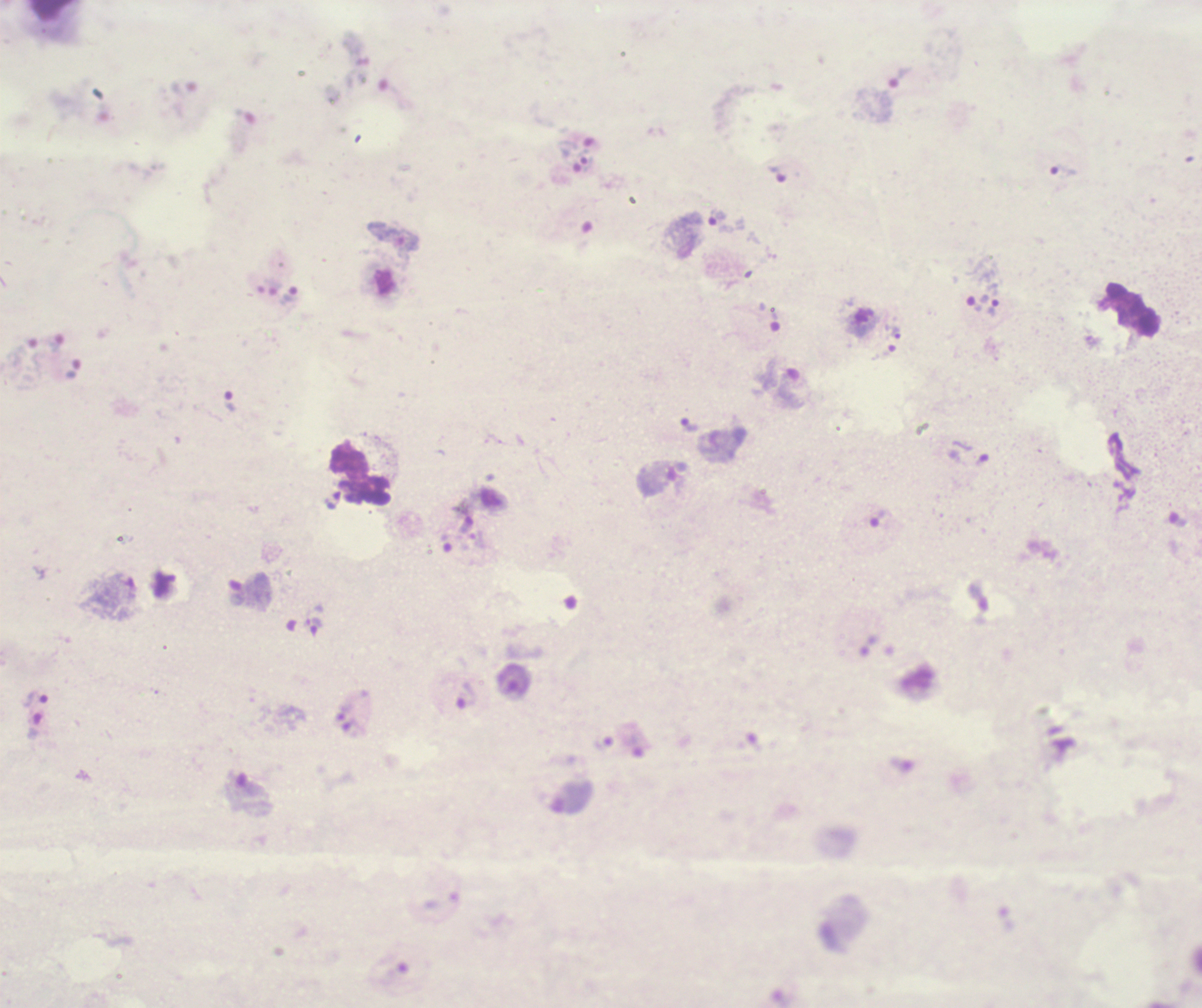

coordinate format = approximate object centers, in pixels from the top-left corner
trophozoite locations = (x=902, y=76), (x=1064, y=171), (x=779, y=174), (x=718, y=217), (x=291, y=295), (x=995, y=308), (x=75, y=368), (x=230, y=402), (x=690, y=425), (x=878, y=519), (x=466, y=695), (x=36, y=700)
leukocyte locations = (x=361, y=474)
preparation = thick smear of blood
context = previously used in an actual diagnosis
magnification = 100x
field of view = one from this slide
coloration quality = bad
background quality = unsatisfactory
result = Plasmodium parasites detected
image size = 1202×1008 pixels
stain = Romanowsky